Locate every Plasmodium parasite.
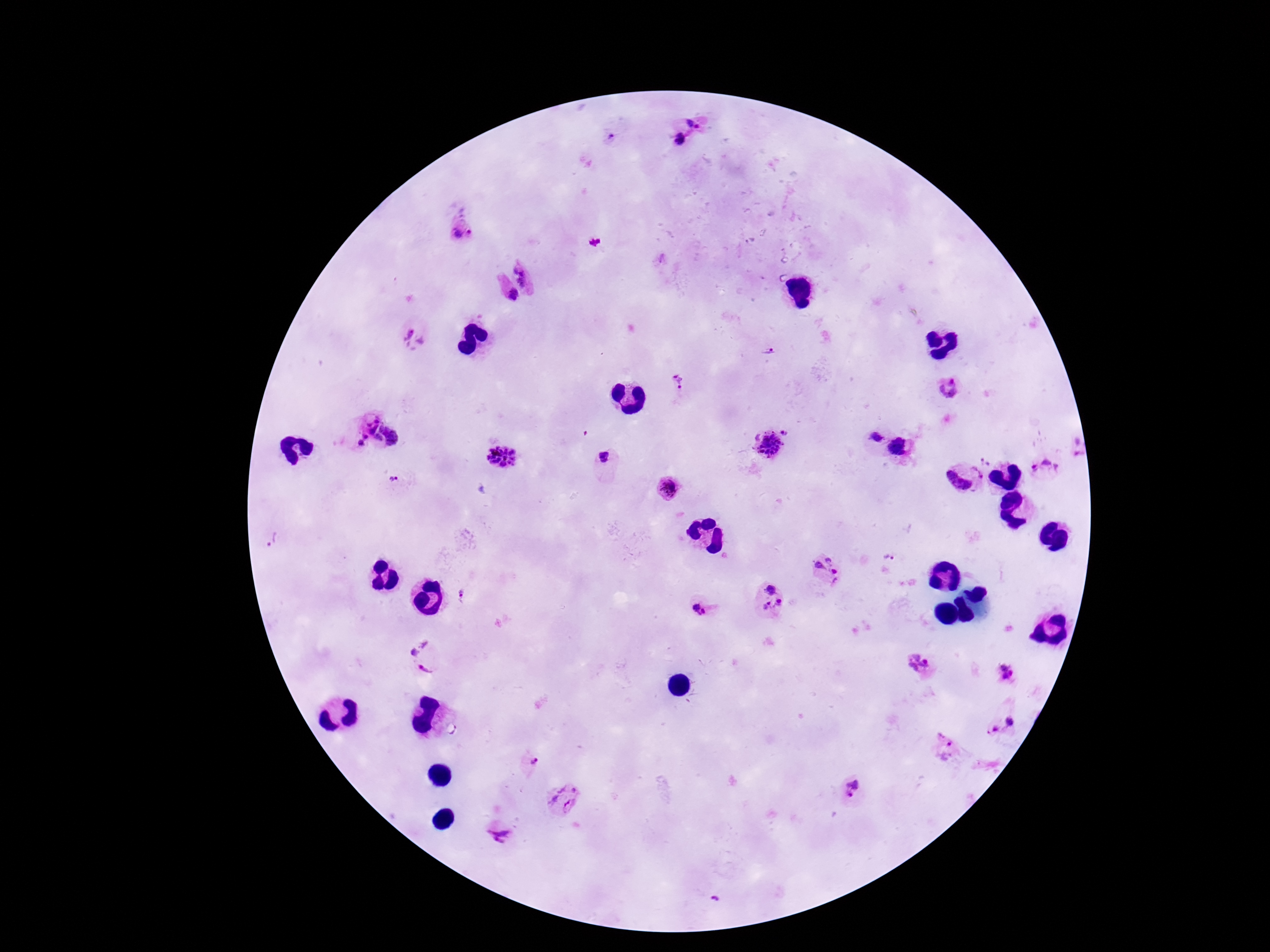

Approximate object centers, in pixels from the top-left corner.
Plasmodium parasites: (x=695, y=123), (x=611, y=137), (x=680, y=138), (x=461, y=235), (x=593, y=240), (x=528, y=269), (x=509, y=296), (x=415, y=338), (x=768, y=353), (x=679, y=381), (x=951, y=388), (x=787, y=431), (x=375, y=434), (x=873, y=438), (x=767, y=444), (x=1076, y=445), (x=898, y=450), (x=502, y=456), (x=604, y=457), (x=987, y=458), (x=980, y=470), (x=1046, y=470), (x=957, y=481), (x=394, y=482), (x=669, y=487), (x=272, y=539), (x=890, y=557), (x=826, y=572), (x=461, y=596), (x=771, y=600), (x=701, y=608), (x=426, y=657), (x=918, y=663), (x=1005, y=672), (x=1012, y=722), (x=991, y=729), (x=947, y=750), (x=534, y=760), (x=850, y=790), (x=561, y=800), (x=500, y=831), (x=715, y=901).

Summary:
  - Image size: 1270×952 pixels
  - Capture: smartphone camera through the microscope eyepiece
  - Field of view: single
  - Preparation: thick peripheral-blood smear
  - Magnification: 100x
  - Stain: Giemsa
  - Patient malaria status: positive